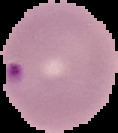

preparation = thin blood smear
image type = segmented cell region on a black background
image size = 118×133 pixels
result = malaria parasites identified